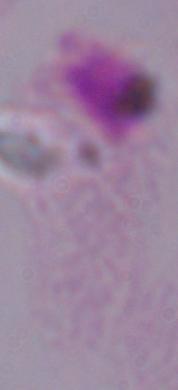
Summary:
  - Modality: photomicrograph
  - Magnification: 1000x
  - Identification: trichomonad